Report the malaria status of this cell.
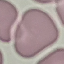

It is uninfected.

Summary:
  - Image type: cell patch, automatically extracted from a larger field of view and resized to 64 × 64 pixels
  - Stain: Giemsa
  - Preparation: thin smear
  - Capture: smartphone through the microscope eyepiece